Classify this cell by malaria status.
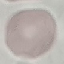

It is uninfected.

{
  "preparation": "thin blood film",
  "capture": "smartphone camera at the microscope eyepiece",
  "stain": "Giemsa",
  "image_type": "cell patch, automatically extracted from a larger field of view and resized to 64 × 64 pixels"
}